Name the cell type shown.
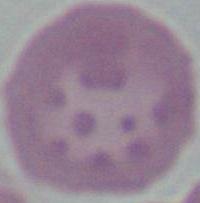

An erythrocyte.

Micrograph. 1000x magnification.